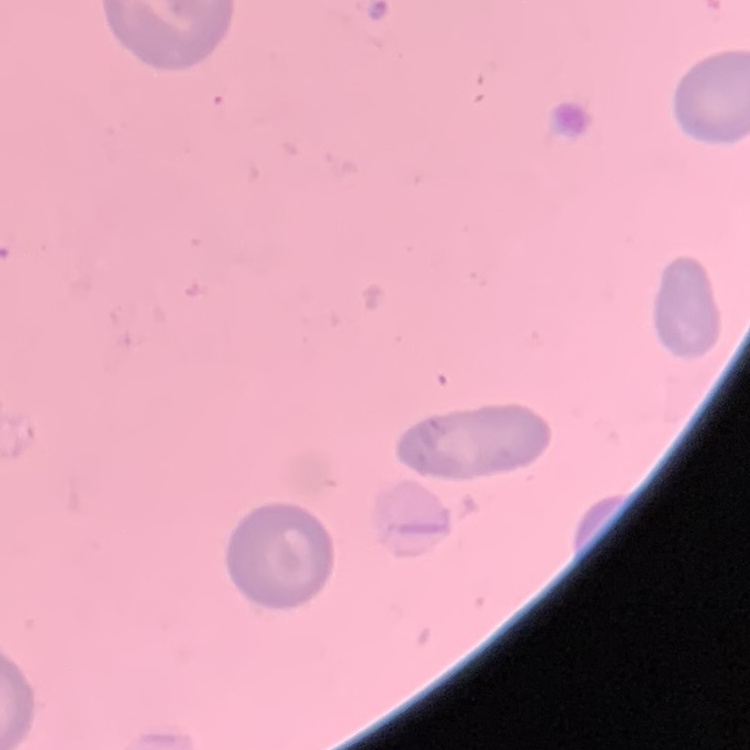

Summary:
  - Erythrocyte morphology: no rouleaux formation
  - Image type: one tile cut from a larger photomicrograph
  - Preparation: thin blood film
  - Stain: Field's or Giemsa